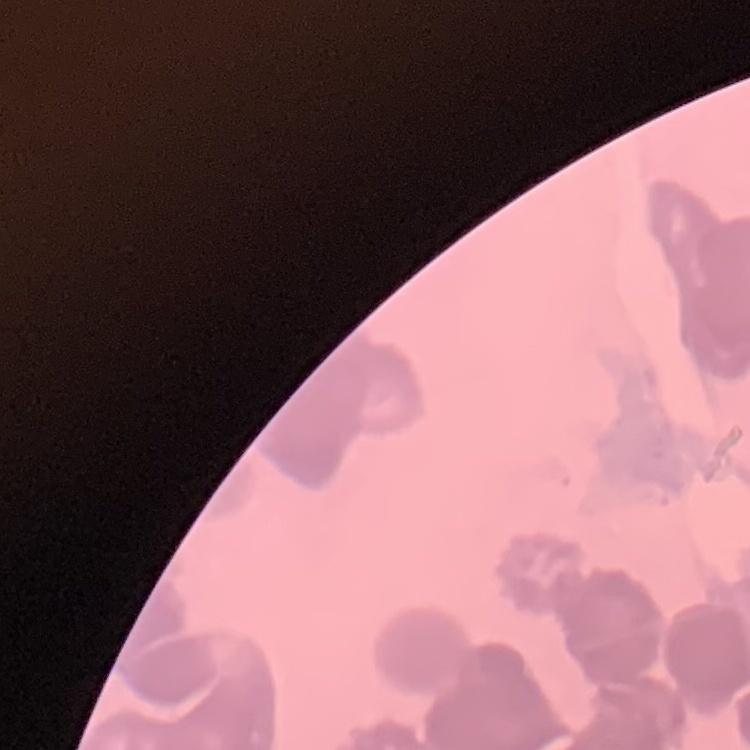

erythrocyte morphology = rouleaux formation
image type = one tile cut from a larger photomicrograph
preparation = thin blood film
stain = Field's or Giemsa